Name the cell type shown.
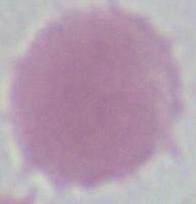
This is an erythrocyte.

{
  "magnification": "1000x",
  "modality": "photomicrograph"
}